Comment on the morphology of the erythrocytes.
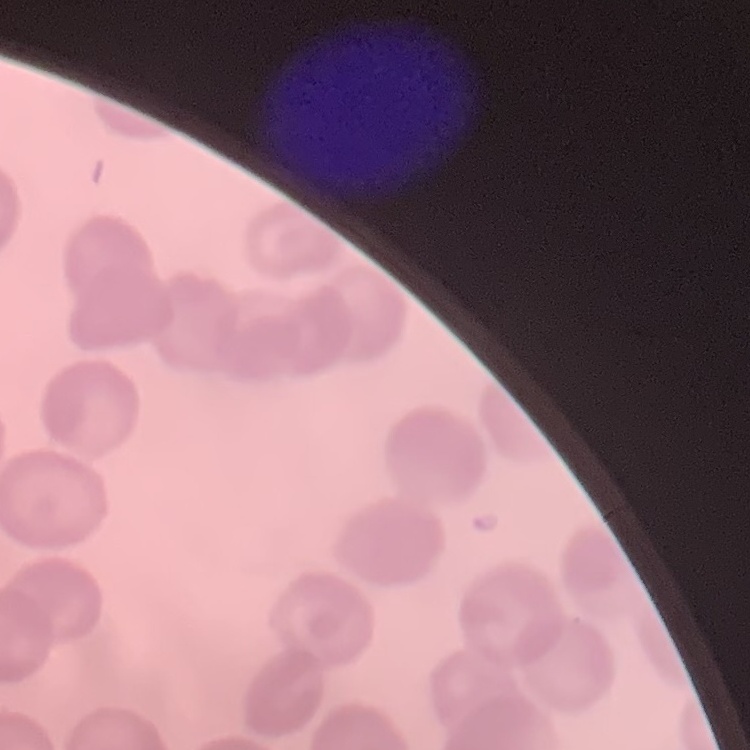
They show no rouleaux formation.

One tile cut from a larger photomicrograph. Thin blood smear. Stained with either Field's or Giemsa.